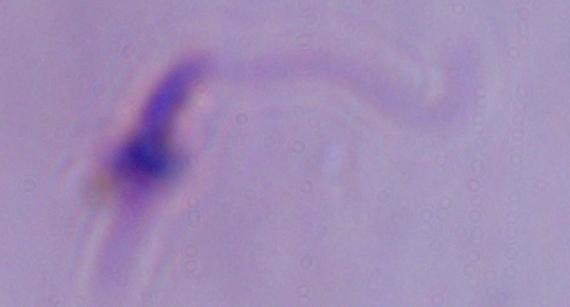
A Leishmania parasite is shown. Captured at 1000x magnification. Micrograph.